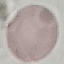

result = no malaria parasites seen
stain = Giemsa
capture = smartphone camera at the microscope eyepiece
image type = cell patch, automatically extracted from a larger field of view and resized to 64 × 64 pixels
preparation = thin blood smear